Locate every blood parasite and identify its species.
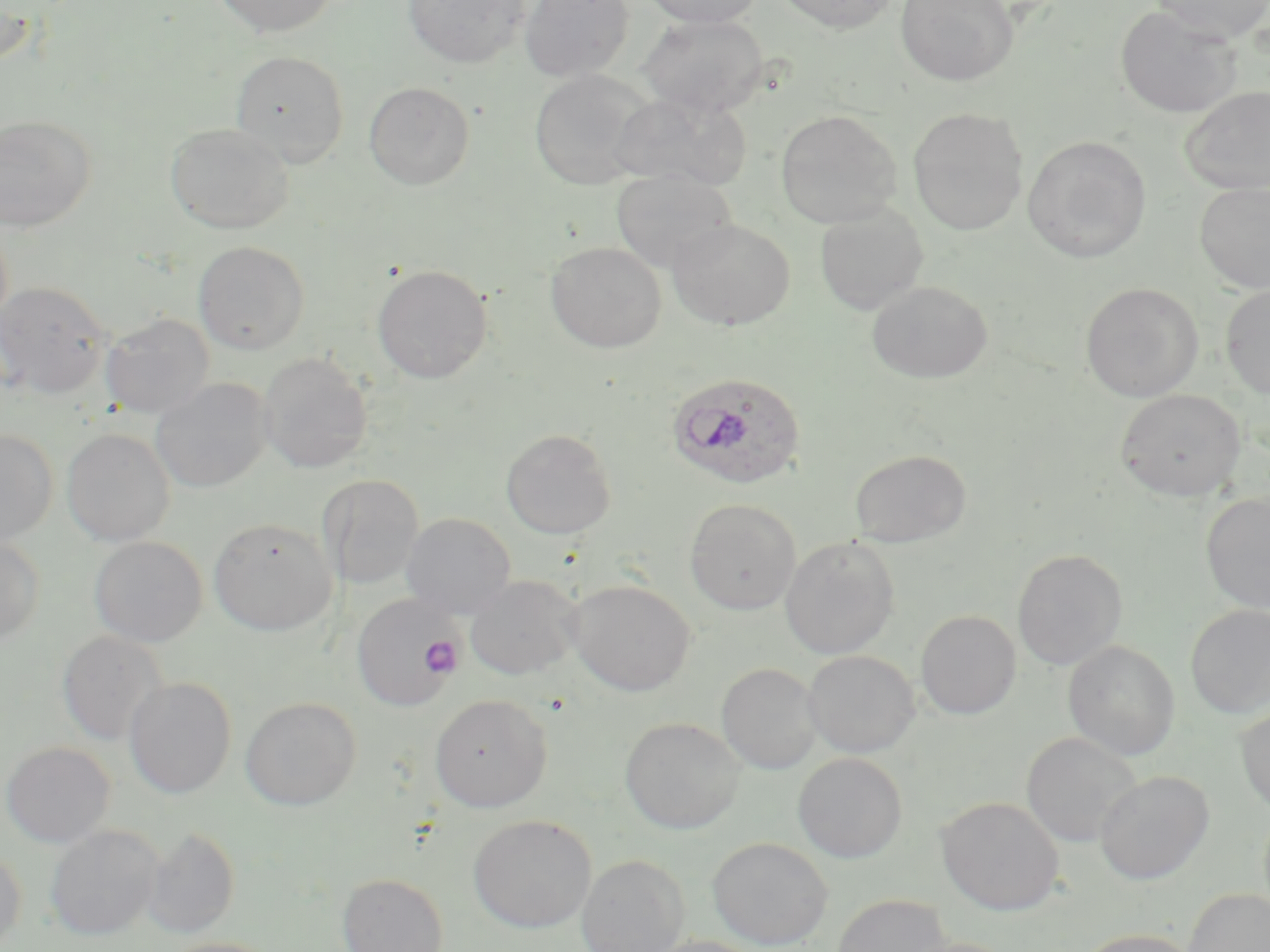

Approximate bounding boxes as (x1,y1)-(x2,y2) corner pairs in pixels.
Plasmodium ovale-infected red blood cells: (666,371)-(807,490).
No Plasmodium falciparum, Plasmodium malariae, Plasmodium vivax, Babesia divergens, or Trypanosoma brucei observed.

slide-level diagnosis = Plasmodium ovale
stain = May-Grünwald-Giemsa
modality = optical microscopy
uninfected red blood cell locations = approximate bounding boxes as (x1,y1)-(x2,y2) corner pairs in pixels: (210,0)-(337,37), (403,0)-(530,67), (519,0)-(635,82), (642,0)-(765,28), (772,0)-(900,34), (895,0)-(1019,86), (1148,0)-(1270,42), (1,2)-(39,69), (1115,6)-(1241,119), (638,14)-(768,117), (230,50)-(350,167), (528,70)-(652,190), (364,81)-(475,190), (1178,87)-(1270,195), (610,91)-(751,191), (908,108)-(1028,235), (775,109)-(902,229), (0,115)-(95,232), (165,123)-(293,234), (1022,135)-(1151,263), (610,168)-(736,273), (1194,182)-(1270,294), (814,203)-(928,315), (667,219)-(795,330), (193,241)-(310,354), (546,241)-(665,353), (372,264)-(492,383), (868,280)-(993,384), (1,281)-(112,398), (1080,282)-(1203,401), (1220,284)-(1270,399), (100,313)-(214,420), (257,353)-(373,474), (150,378)-(272,493), (1115,389)-(1246,501), (62,427)-(175,546), (0,428)-(58,546), (500,429)-(616,539), (849,449)-(971,547), (318,474)-(424,590), (1201,492)-(1270,613), (685,499)-(801,614), (401,512)-(517,618), (208,518)-(337,635), (89,536)-(208,647), (780,536)-(900,660), (0,537)-(45,644), (1012,549)-(1128,670), (464,574)-(581,680), (567,580)-(696,696), (352,593)-(462,711), (1185,604)-(1270,719), (916,611)-(1021,719), (57,630)-(168,747), (1063,640)-(1180,760), (803,650)-(920,758), (717,663)-(823,773), (124,677)-(237,798), (429,693)-(552,813), (240,696)-(362,810), (1235,704)-(1270,817), (620,717)-(745,834), (1021,731)-(1141,848), (1,741)-(115,848), (793,753)-(907,863), (1094,770)-(1213,884), (936,796)-(1064,915), (469,815)-(596,932), (46,825)-(162,939), (142,827)-(240,938), (708,836)-(833,950), (0,847)-(26,952), (576,854)-(689,952), (336,872)-(449,952), (1183,888)-(1270,952), (831,893)-(952,952), (1073,928)-(1203,952), (641,935)-(770,952), (160,937)-(280,952), (902,937)-(1021,952)
platelet locations = approximate bounding boxes as (x1,y1)-(x2,y2) corner pairs in pixels: (420,636)-(463,677)
field of view = one of a larger specimen
preparation = thin blood smear
magnification = 1000x
image size = 1270×952 pixels